Outline each blood parasite and name the species.
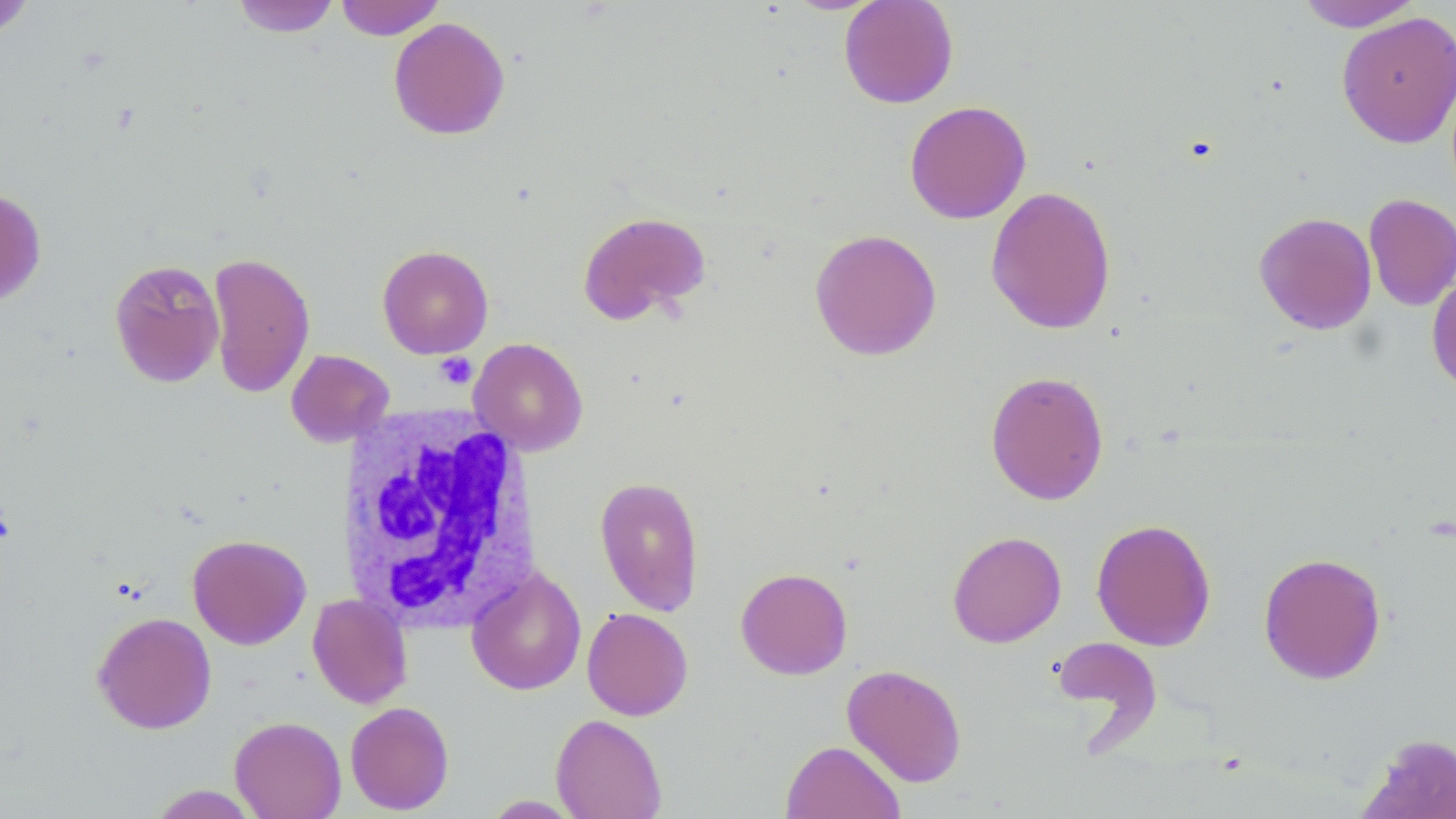

No blood parasites seen.

slide-level diagnosis = negative for blood parasites
platelet locations = approximate bounding boxes as named x1/y1/x2/y2 corners in pixels: (x1=435, y1=352, x2=478, y2=389)
modality = light microscopy
white blood cell locations = approximate bounding boxes as named x1/y1/x2/y2 corners in pixels: (x1=338, y1=404, x2=542, y2=631)
magnification = 1000x
preparation = thin blood smear
stain = May-Grünwald-Giemsa
uninfected red blood cell locations = approximate bounding boxes as named x1/y1/x2/y2 corners in pixels: (x1=231, y1=0, x2=340, y2=38), (x1=334, y1=0, x2=445, y2=40), (x1=838, y1=0, x2=959, y2=109), (x1=0, y1=1, x2=35, y2=38), (x1=1294, y1=1, x2=1425, y2=32), (x1=1336, y1=11, x2=1456, y2=149), (x1=388, y1=16, x2=510, y2=140), (x1=904, y1=100, x2=1032, y2=224), (x1=986, y1=186, x2=1116, y2=335), (x1=0, y1=189, x2=47, y2=305), (x1=1364, y1=193, x2=1456, y2=311), (x1=577, y1=211, x2=711, y2=326), (x1=1254, y1=212, x2=1378, y2=335), (x1=809, y1=228, x2=942, y2=361), (x1=377, y1=245, x2=493, y2=359), (x1=207, y1=251, x2=315, y2=398), (x1=109, y1=259, x2=225, y2=388), (x1=1427, y1=273, x2=1456, y2=394), (x1=469, y1=337, x2=588, y2=456), (x1=285, y1=349, x2=395, y2=448), (x1=985, y1=370, x2=1109, y2=505), (x1=594, y1=476, x2=705, y2=616), (x1=1091, y1=518, x2=1216, y2=651), (x1=947, y1=530, x2=1066, y2=648), (x1=187, y1=534, x2=311, y2=649), (x1=1258, y1=552, x2=1387, y2=684), (x1=735, y1=567, x2=853, y2=680), (x1=466, y1=568, x2=587, y2=695), (x1=308, y1=593, x2=412, y2=709), (x1=582, y1=607, x2=693, y2=721), (x1=92, y1=612, x2=217, y2=734), (x1=1051, y1=636, x2=1162, y2=741), (x1=841, y1=664, x2=967, y2=787), (x1=345, y1=701, x2=454, y2=814), (x1=550, y1=713, x2=667, y2=819), (x1=230, y1=716, x2=346, y2=818), (x1=1359, y1=733, x2=1456, y2=818), (x1=780, y1=740, x2=905, y2=819), (x1=146, y1=785, x2=261, y2=818), (x1=481, y1=795, x2=583, y2=817)
image size = 1456×819 pixels
field of view = single